Classify this cell by malaria status.
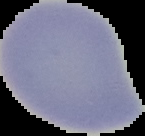

It is uninfected.

Summary:
  - Preparation: thin blood film
  - Image size: 145×136 pixels
  - Image type: segmented cell region with the area outside set to black